Locate every blood parasite and identify its species.
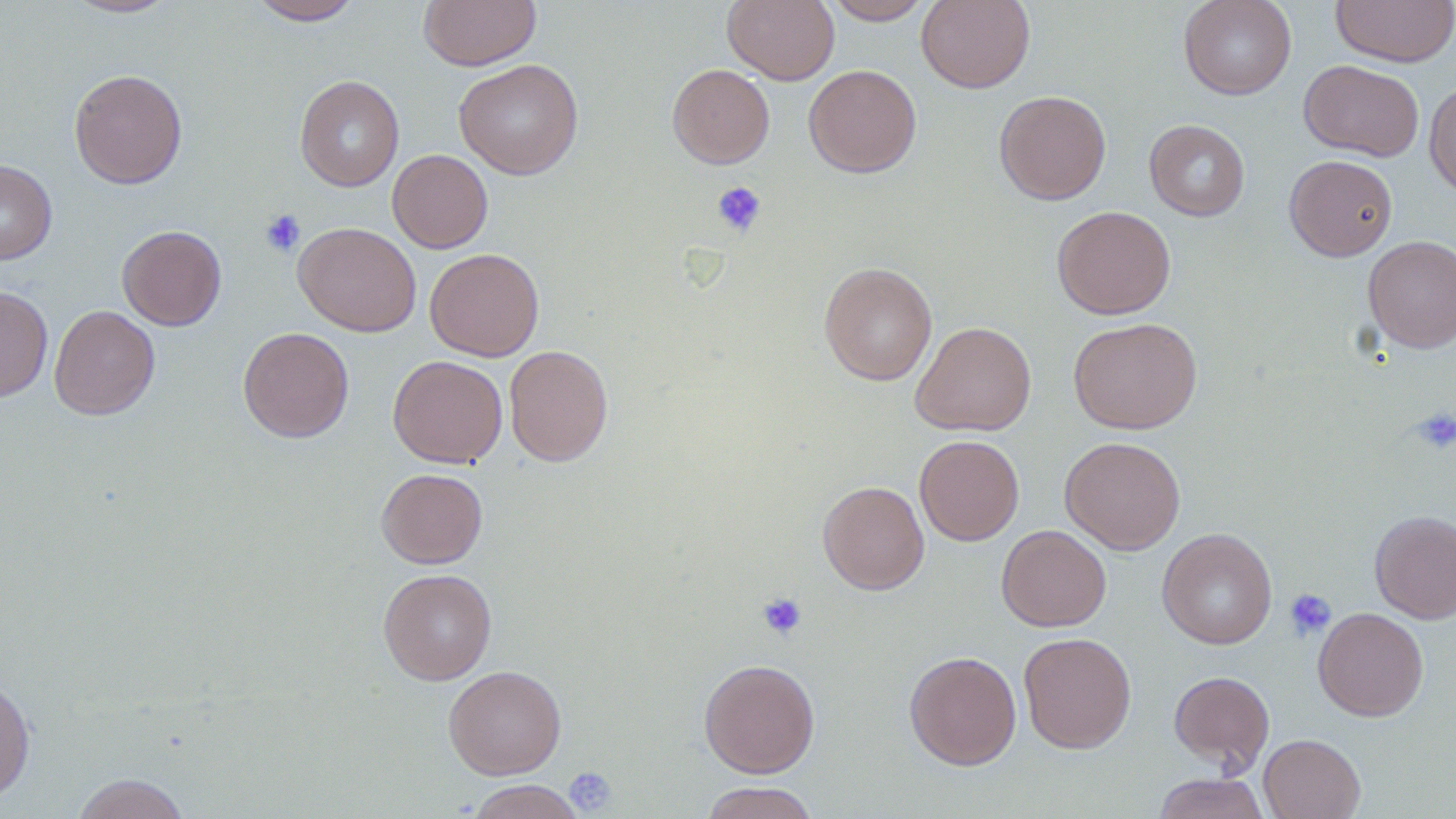
No blood parasites seen.

{
  "slide_level_diagnosis": "negative for blood parasites",
  "platelet_locations": "approximate bounding boxes as named x1/y1/x2/y2 corners in pixels: (x1=712, y1=182, x2=766, y2=237), (x1=260, y1=209, x2=305, y2=257), (x1=1411, y1=406, x2=1456, y2=454), (x1=1284, y1=588, x2=1337, y2=640), (x1=756, y1=592, x2=807, y2=640), (x1=564, y1=767, x2=618, y2=815)",
  "modality": "light microscopy",
  "magnification": "1000x",
  "field_of_view": "single",
  "uninfected_red_blood_cell_locations": "approximate bounding boxes as named x1/y1/x2/y2 corners in pixels: (x1=63, y1=0, x2=179, y2=18), (x1=247, y1=0, x2=364, y2=25), (x1=417, y1=0, x2=542, y2=71), (x1=722, y1=0, x2=839, y2=85), (x1=822, y1=0, x2=935, y2=25), (x1=916, y1=0, x2=1035, y2=93), (x1=1178, y1=0, x2=1297, y2=100), (x1=1330, y1=0, x2=1456, y2=68), (x1=453, y1=59, x2=583, y2=180), (x1=1299, y1=60, x2=1424, y2=161), (x1=667, y1=63, x2=775, y2=169), (x1=803, y1=64, x2=921, y2=178), (x1=68, y1=68, x2=188, y2=189), (x1=294, y1=74, x2=405, y2=191), (x1=1423, y1=79, x2=1456, y2=197), (x1=994, y1=89, x2=1111, y2=205), (x1=1144, y1=119, x2=1250, y2=221), (x1=387, y1=149, x2=493, y2=253), (x1=1284, y1=155, x2=1397, y2=261), (x1=0, y1=159, x2=57, y2=265), (x1=1052, y1=206, x2=1175, y2=319), (x1=293, y1=222, x2=421, y2=337), (x1=117, y1=224, x2=227, y2=330), (x1=1362, y1=235, x2=1456, y2=353), (x1=425, y1=248, x2=544, y2=362), (x1=819, y1=262, x2=937, y2=386), (x1=0, y1=285, x2=53, y2=402), (x1=49, y1=305, x2=160, y2=420), (x1=1068, y1=317, x2=1202, y2=435), (x1=911, y1=321, x2=1036, y2=436), (x1=237, y1=326, x2=354, y2=443), (x1=504, y1=344, x2=614, y2=466), (x1=388, y1=355, x2=508, y2=468), (x1=914, y1=435, x2=1025, y2=546), (x1=1059, y1=436, x2=1186, y2=555), (x1=376, y1=468, x2=488, y2=569), (x1=818, y1=480, x2=930, y2=594), (x1=1369, y1=509, x2=1456, y2=623), (x1=996, y1=525, x2=1111, y2=631), (x1=1157, y1=528, x2=1278, y2=649), (x1=378, y1=568, x2=497, y2=685), (x1=1313, y1=607, x2=1429, y2=721), (x1=1018, y1=632, x2=1137, y2=753), (x1=904, y1=650, x2=1022, y2=769), (x1=698, y1=658, x2=820, y2=778), (x1=443, y1=665, x2=567, y2=780), (x1=1168, y1=670, x2=1275, y2=773), (x1=0, y1=675, x2=36, y2=804), (x1=1258, y1=733, x2=1366, y2=819), (x1=1151, y1=772, x2=1272, y2=819), (x1=71, y1=773, x2=191, y2=819), (x1=465, y1=779, x2=586, y2=819), (x1=697, y1=781, x2=821, y2=819)",
  "stain": "May-Grünwald-Giemsa",
  "image_size": "1456×819 pixels",
  "preparation": "thin blood film"
}